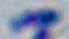
modality: micrograph
identification: Toxoplasma gondii
magnification: 1000x